Locate leukocytes (white blood cells).
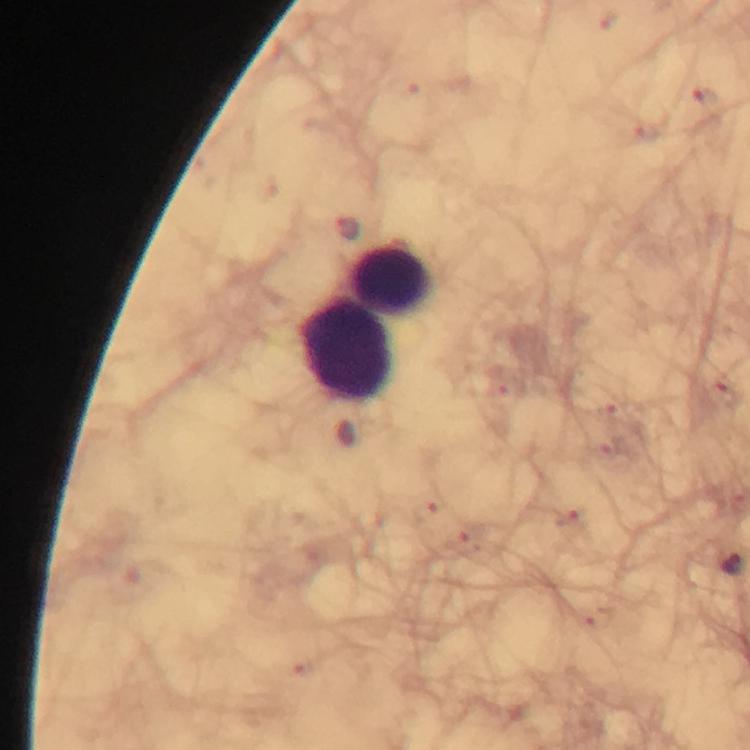

Approximate centers as [x, y] in pixels.
Leukocytes: [391, 280], [347, 350].

Summary:
  - Capture: smartphone photograph through a microscope
  - Stain: Giemsa
  - Malaria parasites: none detected
  - Immersion oil: used
  - Cropped from: one field of view
  - Magnification: 100x
  - Context: from a malaria diagnostic workup
  - Preparation: thick smear
  - Image size: 750×750 pixels